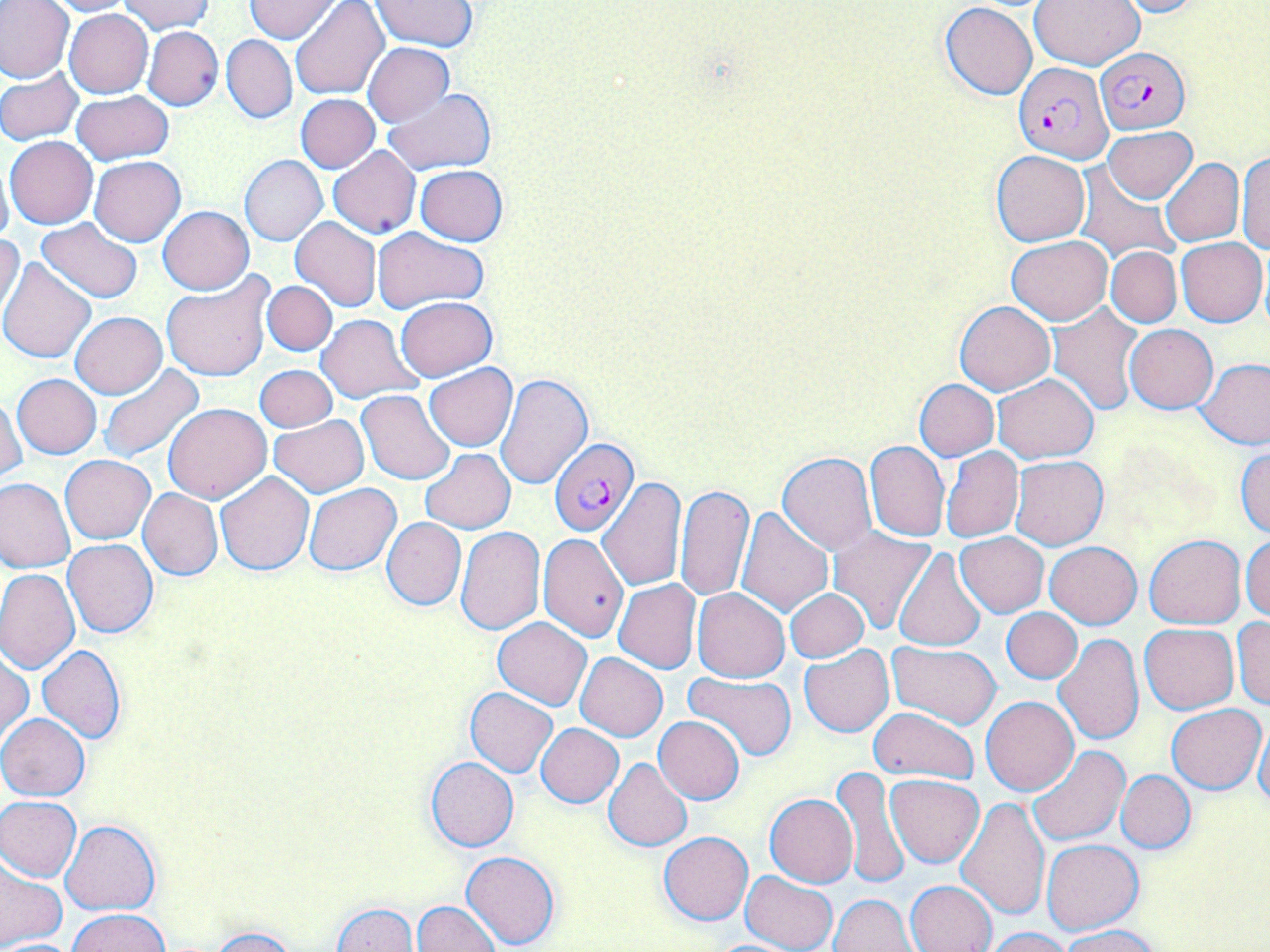
{
  "plasmodium_falciparum_infected_red_blood_cell_locations": "approximate bounding boxes as (x1,y1)-(x2,y2) corner pairs in pixels: (1096,46)-(1189,134), (1012,63)-(1113,163), (548,438)-(636,537)",
  "slide_level_diagnosis": "Plasmodium falciparum",
  "field_of_view": "one of a larger specimen",
  "image_size": "1270×952 pixels",
  "magnification": "1000x",
  "preparation": "thin blood film",
  "modality": "optical microscopy",
  "uninfected_red_blood_cell_locations": "approximate bounding boxes as (x1,y1)-(x2,y2) corner pairs in pixels: (1,0)-(75,84), (39,0)-(136,16), (244,0)-(339,43), (1029,0)-(1146,70), (1111,0)-(1211,18), (118,1)-(214,36), (291,1)-(388,103), (372,1)-(478,51), (939,4)-(1036,99), (64,9)-(153,98), (142,26)-(223,111), (222,34)-(297,124), (362,42)-(454,127), (0,68)-(84,145), (383,88)-(496,174), (71,92)-(174,165), (296,93)-(380,172), (1103,126)-(1197,203), (5,136)-(98,229), (328,146)-(421,239), (990,149)-(1091,247), (1235,151)-(1270,254), (0,155)-(14,251), (240,155)-(328,246), (89,156)-(184,246), (1160,157)-(1243,246), (415,165)-(508,245), (1076,169)-(1179,262), (158,206)-(253,294), (290,217)-(382,312), (36,218)-(143,303), (372,227)-(488,314), (0,233)-(25,320), (1006,236)-(1111,324), (1176,239)-(1266,326), (1106,246)-(1182,328), (0,255)-(97,362), (160,273)-(274,382), (262,280)-(336,356), (396,297)-(497,381), (955,301)-(1054,394), (1048,305)-(1145,416), (71,312)-(167,398), (316,314)-(422,406), (1125,324)-(1217,413), (1197,358)-(1270,448), (424,364)-(517,452), (255,365)-(337,433), (99,366)-(206,463), (495,373)-(592,490), (993,373)-(1098,463), (12,374)-(101,459), (914,378)-(999,460), (357,389)-(457,485), (0,393)-(24,481), (162,403)-(272,504), (270,416)-(368,497), (864,440)-(949,542), (1234,445)-(1270,538), (941,446)-(1023,542), (420,449)-(515,533), (778,453)-(877,555), (61,455)-(154,543), (1010,456)-(1108,549), (215,471)-(313,574), (0,477)-(75,574), (598,479)-(687,590), (304,483)-(401,575), (675,484)-(754,601), (138,489)-(223,580), (735,506)-(834,617), (382,518)-(466,610), (826,526)-(937,633), (456,527)-(544,634), (539,533)-(629,642), (955,533)-(1048,617), (1144,534)-(1246,629), (1241,534)-(1270,623), (63,539)-(158,638), (1045,541)-(1141,628), (893,547)-(987,652), (0,569)-(80,674), (614,578)-(701,674), (692,588)-(790,682), (785,588)-(870,663), (1001,608)-(1081,684), (493,617)-(592,709), (1231,617)-(1270,709), (1140,623)-(1238,713), (1053,633)-(1145,747), (887,641)-(1000,728), (799,645)-(894,737), (38,646)-(126,744), (1,647)-(31,748), (576,652)-(667,741), (683,673)-(797,765), (464,687)-(557,778), (982,695)-(1078,796), (1167,705)-(1265,793), (867,707)-(980,783), (0,714)-(89,800), (654,715)-(746,804), (1255,717)-(1269,812), (535,723)-(624,807), (1025,745)-(1130,847), (603,757)-(692,852), (425,758)-(518,852), (834,765)-(908,892), (1117,770)-(1195,852), (885,774)-(984,867), (765,793)-(857,887), (1,795)-(82,881), (957,797)-(1049,920), (60,820)-(161,916), (659,830)-(753,925), (1041,838)-(1143,933), (462,850)-(561,950), (0,861)-(66,947), (740,870)-(838,952), (906,879)-(998,952), (831,893)-(917,952), (412,901)-(501,952), (330,903)-(419,952), (68,909)-(172,952), (1060,925)-(1164,952), (981,926)-(1076,951), (204,927)-(300,952), (0,938)-(80,951)",
  "stain": "May-Grünwald-Giemsa"
}